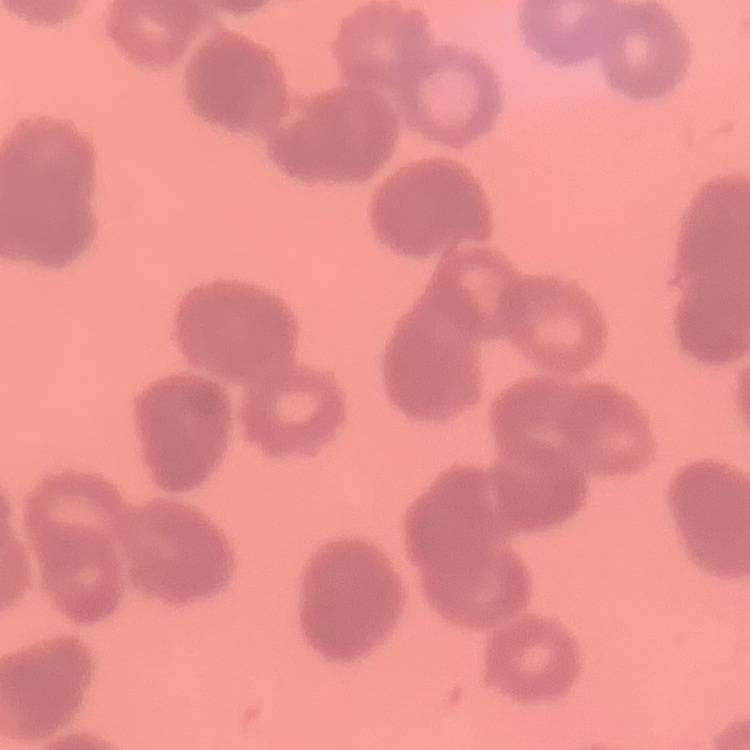 The erythrocytes show rouleaux formation. Square crop of a larger photomicrograph. Field's or Giemsa stain. Thin blood smear.